Locate every Trypanosoma brucei.
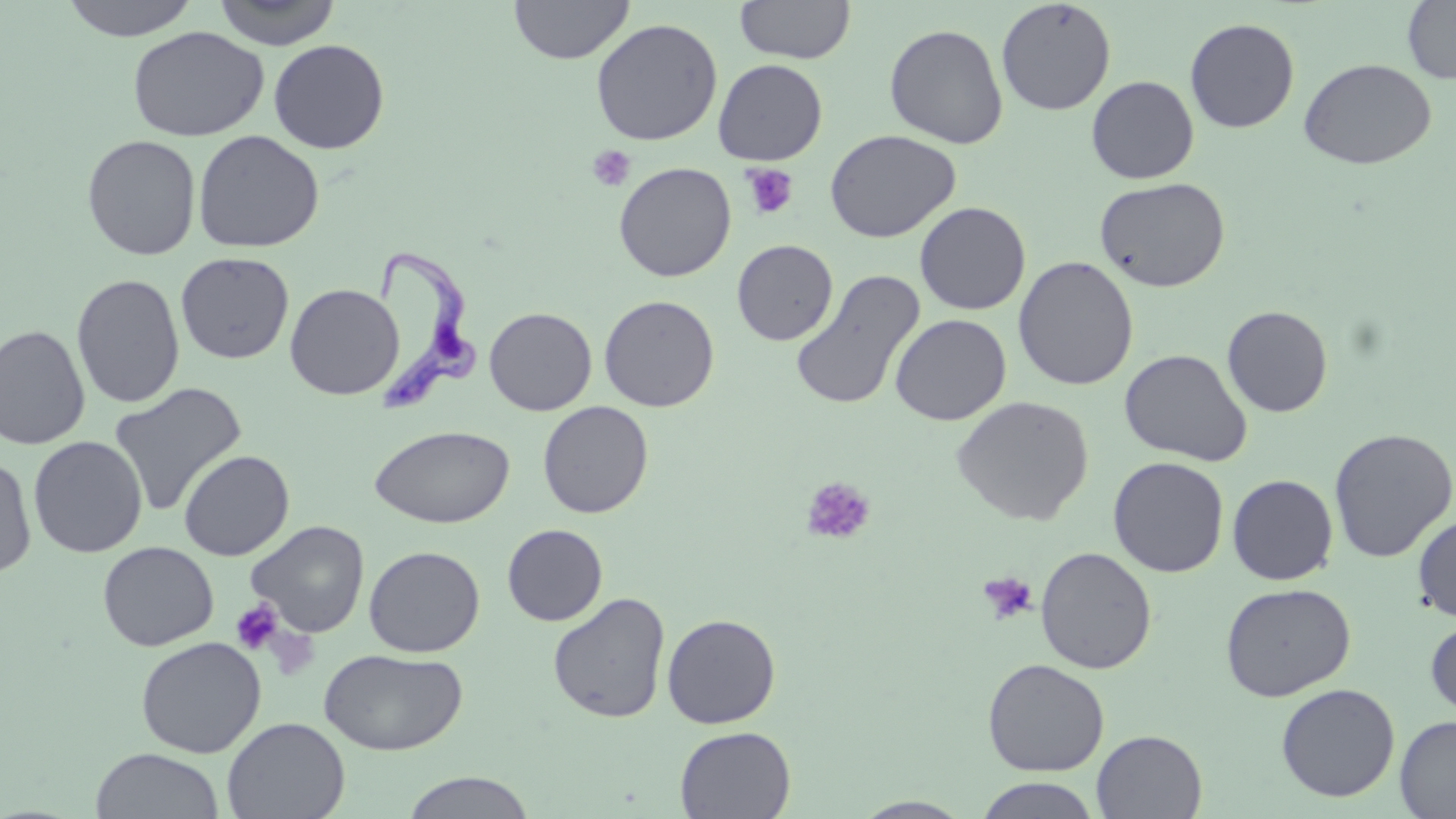

Approximate bounding boxes as named x1/y1/x2/y2 corners in pixels.
Trypanosoma brucei: (x1=370, y1=245, x2=482, y2=414).

Platelet locations: (x1=587, y1=145, x2=636, y2=192), (x1=740, y1=162, x2=799, y2=221), (x1=801, y1=476, x2=876, y2=544), (x1=977, y1=570, x2=1038, y2=625), (x1=229, y1=599, x2=285, y2=656). Uninfected red blood cell locations: (x1=59, y1=0, x2=201, y2=41), (x1=211, y1=0, x2=342, y2=49), (x1=509, y1=0, x2=634, y2=64), (x1=735, y1=0, x2=856, y2=64), (x1=996, y1=0, x2=1116, y2=116), (x1=1402, y1=0, x2=1456, y2=84), (x1=590, y1=17, x2=723, y2=146), (x1=1185, y1=18, x2=1300, y2=133), (x1=884, y1=23, x2=1009, y2=149), (x1=127, y1=26, x2=269, y2=142), (x1=268, y1=39, x2=390, y2=154), (x1=1298, y1=58, x2=1436, y2=170), (x1=712, y1=59, x2=827, y2=165), (x1=1086, y1=76, x2=1199, y2=184), (x1=824, y1=129, x2=961, y2=243), (x1=192, y1=130, x2=324, y2=253), (x1=82, y1=134, x2=201, y2=260), (x1=613, y1=161, x2=737, y2=282), (x1=1093, y1=176, x2=1231, y2=293), (x1=915, y1=201, x2=1031, y2=315), (x1=732, y1=239, x2=838, y2=345), (x1=175, y1=251, x2=294, y2=364), (x1=1012, y1=256, x2=1139, y2=390), (x1=789, y1=269, x2=925, y2=412), (x1=71, y1=273, x2=185, y2=408), (x1=284, y1=283, x2=404, y2=400), (x1=599, y1=295, x2=719, y2=412), (x1=1222, y1=305, x2=1333, y2=417), (x1=484, y1=307, x2=597, y2=416), (x1=890, y1=313, x2=1012, y2=425), (x1=0, y1=324, x2=91, y2=450), (x1=1119, y1=348, x2=1252, y2=466), (x1=108, y1=382, x2=247, y2=517), (x1=951, y1=395, x2=1094, y2=525), (x1=537, y1=401, x2=654, y2=519), (x1=369, y1=425, x2=515, y2=529), (x1=1327, y1=428, x2=1456, y2=563), (x1=28, y1=436, x2=147, y2=558), (x1=178, y1=450, x2=294, y2=561), (x1=0, y1=454, x2=37, y2=577), (x1=1108, y1=456, x2=1229, y2=577), (x1=1227, y1=474, x2=1338, y2=585), (x1=1413, y1=513, x2=1456, y2=622), (x1=246, y1=520, x2=369, y2=637), (x1=502, y1=524, x2=608, y2=626), (x1=97, y1=541, x2=218, y2=651), (x1=364, y1=545, x2=485, y2=657), (x1=1035, y1=546, x2=1157, y2=674), (x1=1219, y1=582, x2=1356, y2=702), (x1=547, y1=591, x2=671, y2=724), (x1=662, y1=613, x2=781, y2=728), (x1=1425, y1=615, x2=1456, y2=721), (x1=135, y1=636, x2=267, y2=758), (x1=319, y1=648, x2=468, y2=755), (x1=982, y1=658, x2=1109, y2=777), (x1=1275, y1=682, x2=1400, y2=802), (x1=1395, y1=715, x2=1456, y2=818), (x1=222, y1=716, x2=350, y2=819), (x1=674, y1=725, x2=796, y2=819), (x1=1092, y1=730, x2=1207, y2=819), (x1=90, y1=747, x2=225, y2=819), (x1=400, y1=771, x2=537, y2=818), (x1=974, y1=777, x2=1102, y2=819), (x1=852, y1=796, x2=976, y2=818). Slide-level diagnosis: Trypanosoma brucei. Image is 1456×819 pixels. Thin blood film. Optical microscopy. May-Grünwald-Giemsa stain. 1000x magnification. Single field of view.